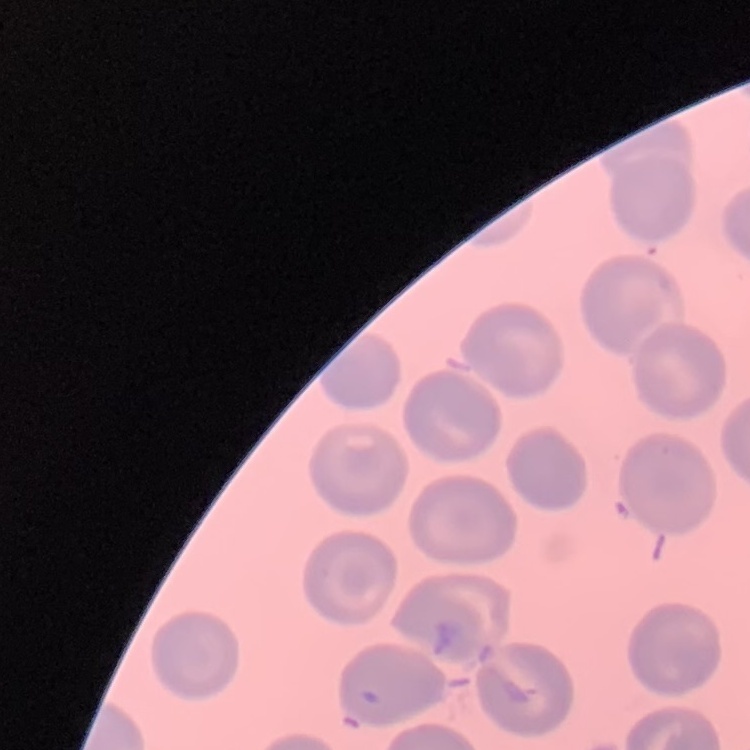

{
  "erythrocyte_morphology": "no rouleaux formation",
  "preparation": "thin blood film",
  "image_type": "one tile cut from a larger photomicrograph",
  "stain": "Field's or Giemsa"
}